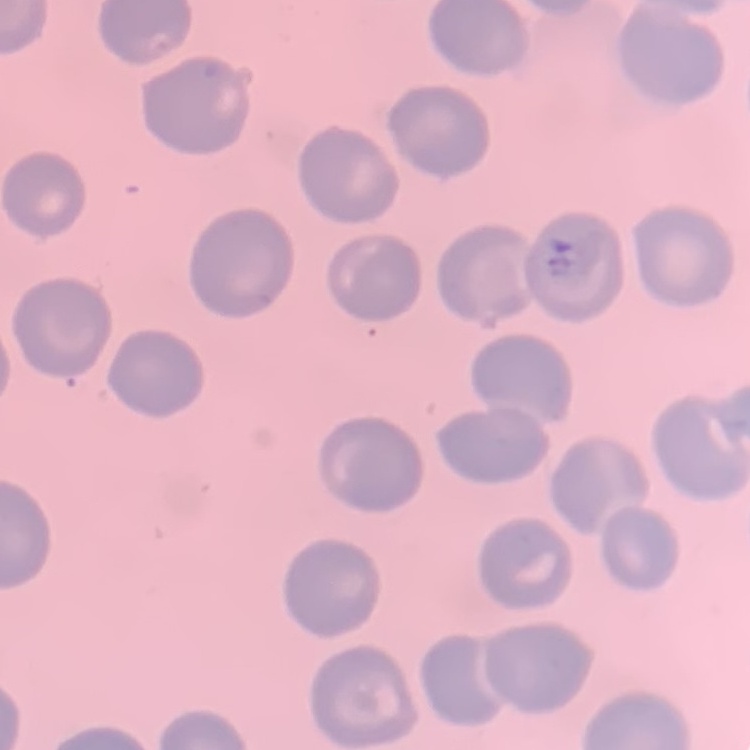

Summary:
  - Erythrocyte morphology: no rouleaux formation
  - Stain: Field's or Giemsa
  - Preparation: thin peripheral smear
  - Image type: square crop of a larger photomicrograph